Look for Plasmodium parasites.
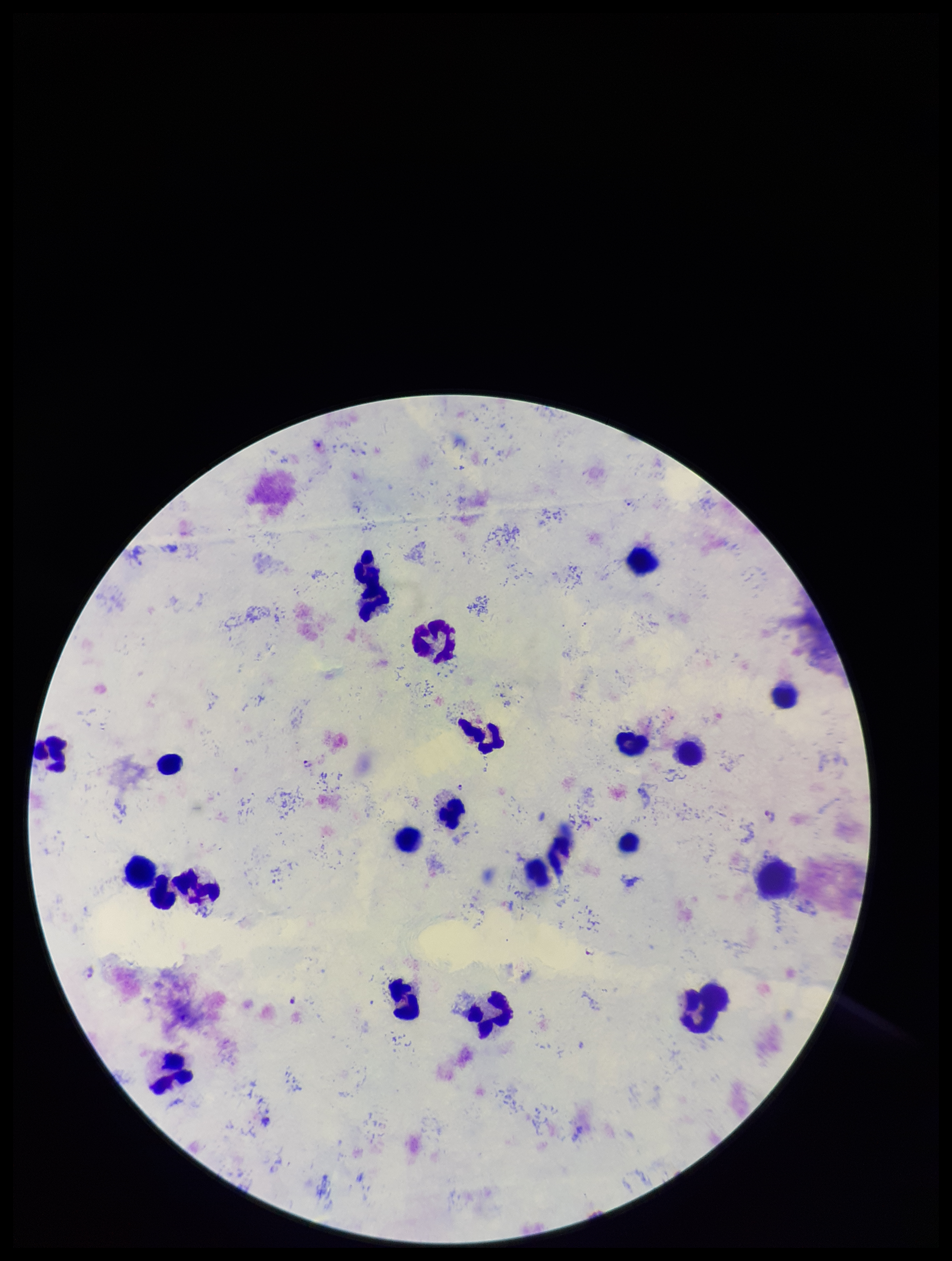
Detected.

Summary:
  - Species reported for this patient: Plasmodium falciparum
  - Field of view: single
  - Preparation: thick blood smear
  - Stain: Giemsa
  - Parasite count: 4
  - Capture: smartphone photograph through the microscope eyepiece
  - Patient malaria status: positive
  - Leukocyte count: 22
  - Image size: 952×1261 pixels